Identify the parasite.
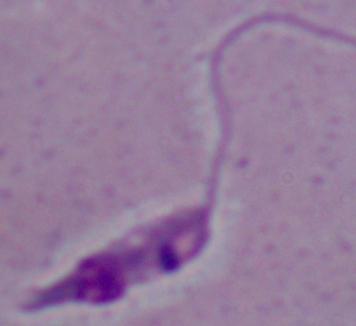
This is Leishmania.

{
  "modality": "photomicrograph",
  "magnification": "1000x"
}